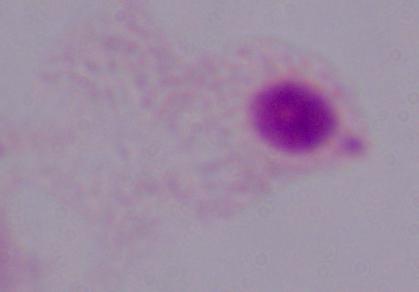

modality = micrograph
identification = trichomonad
magnification = 1000x